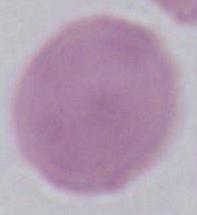
{
  "modality": "photomicrograph",
  "identification": "erythrocyte",
  "magnification": "1000x"
}